State the blood parasite species.
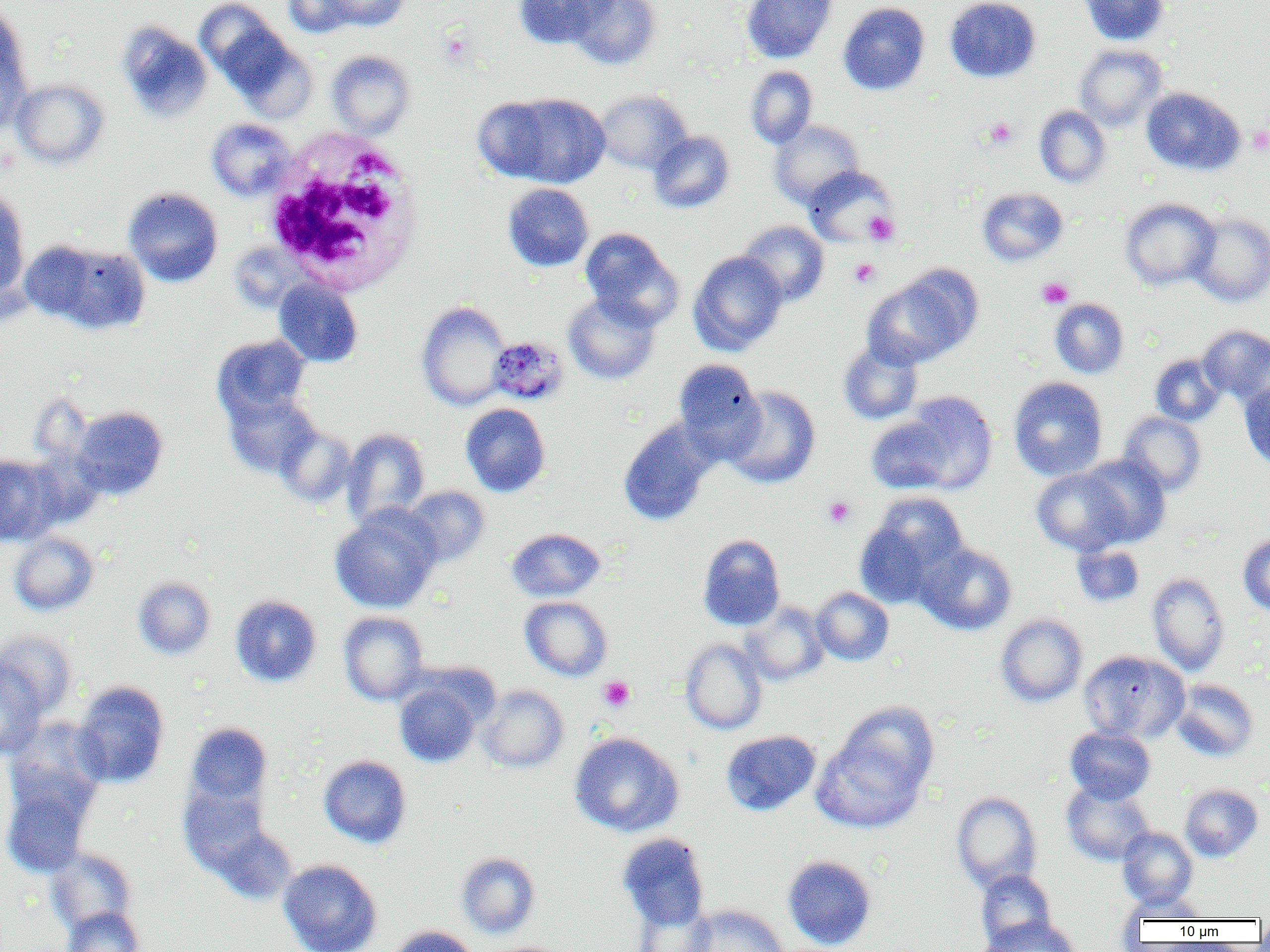

Plasmodium malariae.

image size = 1270×952 pixels
white blood cell locations = approximate bounding boxes as named x1/y1/x2/y2 corners in pixels: (x1=264, y1=132, x2=425, y2=296)
platelet locations = approximate bounding boxes as named x1/y1/x2/y2 corners in pixels: (x1=439, y1=30, x2=474, y2=65), (x1=985, y1=118, x2=1017, y2=149), (x1=1248, y1=126, x2=1270, y2=154), (x1=864, y1=211, x2=899, y2=245), (x1=849, y1=258, x2=880, y2=287), (x1=1037, y1=277, x2=1074, y2=309), (x1=823, y1=497, x2=855, y2=529), (x1=598, y1=675, x2=635, y2=712)
Plasmodium malariae-infected red blood cell locations = approximate bounding boxes as named x1/y1/x2/y2 corners in pixels: (x1=489, y1=337, x2=568, y2=405)
field of view = one of a larger specimen
uninfected red blood cell locations = approximate bounding boxes as named x1/y1/x2/y2 corners in pixels: (x1=195, y1=0, x2=286, y2=86), (x1=282, y1=0, x2=359, y2=37), (x1=326, y1=0, x2=409, y2=31), (x1=513, y1=0, x2=612, y2=49), (x1=566, y1=0, x2=662, y2=70), (x1=741, y1=0, x2=838, y2=63), (x1=944, y1=0, x2=1041, y2=83), (x1=1078, y1=0, x2=1169, y2=45), (x1=838, y1=2, x2=930, y2=95), (x1=0, y1=6, x2=33, y2=131), (x1=117, y1=22, x2=213, y2=122), (x1=219, y1=26, x2=317, y2=122), (x1=1075, y1=44, x2=1167, y2=131), (x1=326, y1=50, x2=415, y2=138), (x1=745, y1=66, x2=817, y2=148), (x1=11, y1=79, x2=109, y2=169), (x1=1141, y1=87, x2=1245, y2=176), (x1=595, y1=89, x2=693, y2=174), (x1=488, y1=92, x2=610, y2=189), (x1=1034, y1=106, x2=1111, y2=187), (x1=207, y1=118, x2=296, y2=200), (x1=769, y1=120, x2=865, y2=208), (x1=648, y1=131, x2=734, y2=213), (x1=803, y1=166, x2=897, y2=246), (x1=503, y1=183, x2=594, y2=271), (x1=0, y1=187, x2=30, y2=301), (x1=123, y1=187, x2=223, y2=287), (x1=977, y1=188, x2=1067, y2=266), (x1=1120, y1=198, x2=1219, y2=290), (x1=1188, y1=212, x2=1270, y2=306), (x1=737, y1=220, x2=829, y2=307), (x1=580, y1=228, x2=682, y2=329), (x1=35, y1=241, x2=152, y2=334), (x1=688, y1=250, x2=788, y2=356), (x1=862, y1=270, x2=978, y2=368), (x1=273, y1=279, x2=363, y2=367), (x1=563, y1=292, x2=661, y2=385), (x1=1050, y1=298, x2=1129, y2=378), (x1=415, y1=301, x2=511, y2=411), (x1=1199, y1=325, x2=1270, y2=403), (x1=212, y1=334, x2=311, y2=421), (x1=838, y1=340, x2=923, y2=424), (x1=1150, y1=353, x2=1226, y2=426), (x1=673, y1=358, x2=765, y2=459), (x1=1008, y1=376, x2=1108, y2=480), (x1=1240, y1=381, x2=1270, y2=471), (x1=723, y1=386, x2=821, y2=488), (x1=223, y1=390, x2=321, y2=479), (x1=899, y1=391, x2=998, y2=494), (x1=460, y1=403, x2=550, y2=497), (x1=71, y1=406, x2=168, y2=499), (x1=1119, y1=412, x2=1206, y2=495), (x1=865, y1=416, x2=955, y2=494), (x1=618, y1=418, x2=717, y2=526), (x1=275, y1=424, x2=356, y2=508), (x1=341, y1=428, x2=430, y2=528), (x1=0, y1=454, x2=60, y2=546), (x1=1078, y1=454, x2=1172, y2=547), (x1=1031, y1=467, x2=1130, y2=556), (x1=403, y1=486, x2=490, y2=567), (x1=855, y1=494, x2=968, y2=607), (x1=329, y1=506, x2=441, y2=614), (x1=506, y1=527, x2=606, y2=601), (x1=8, y1=532, x2=99, y2=616), (x1=1238, y1=533, x2=1270, y2=616), (x1=697, y1=534, x2=785, y2=631), (x1=916, y1=543, x2=1017, y2=635), (x1=1071, y1=543, x2=1144, y2=607), (x1=1147, y1=572, x2=1230, y2=674), (x1=133, y1=576, x2=216, y2=659), (x1=811, y1=587, x2=894, y2=665), (x1=230, y1=594, x2=322, y2=687), (x1=519, y1=596, x2=613, y2=681), (x1=741, y1=601, x2=829, y2=685), (x1=338, y1=611, x2=429, y2=705), (x1=995, y1=613, x2=1087, y2=706), (x1=1, y1=630, x2=78, y2=718), (x1=680, y1=638, x2=767, y2=734), (x1=1078, y1=650, x2=1188, y2=743), (x1=0, y1=660, x2=48, y2=760), (x1=394, y1=678, x2=485, y2=767), (x1=1171, y1=679, x2=1259, y2=762), (x1=72, y1=681, x2=169, y2=788), (x1=478, y1=685, x2=569, y2=773), (x1=812, y1=708, x2=937, y2=832), (x1=185, y1=722, x2=273, y2=809), (x1=1065, y1=726, x2=1155, y2=803), (x1=720, y1=729, x2=821, y2=816), (x1=569, y1=731, x2=684, y2=837), (x1=318, y1=755, x2=412, y2=848), (x1=0, y1=767, x2=98, y2=878), (x1=1062, y1=781, x2=1155, y2=866), (x1=179, y1=783, x2=271, y2=876), (x1=1179, y1=784, x2=1263, y2=862), (x1=951, y1=791, x2=1042, y2=893), (x1=213, y1=825, x2=297, y2=904), (x1=1117, y1=827, x2=1198, y2=908), (x1=617, y1=833, x2=710, y2=931), (x1=46, y1=847, x2=137, y2=934), (x1=456, y1=851, x2=541, y2=938), (x1=782, y1=854, x2=876, y2=950), (x1=278, y1=859, x2=382, y2=952), (x1=975, y1=868, x2=1056, y2=948), (x1=1119, y1=893, x2=1211, y2=923), (x1=632, y1=899, x2=716, y2=952), (x1=685, y1=904, x2=788, y2=952), (x1=61, y1=906, x2=144, y2=952), (x1=981, y1=915, x2=1081, y2=952), (x1=386, y1=925, x2=478, y2=952)
magnification = 1000x
modality = light microscopy
preparation = thin blood smear